Give the extent of all Plasmodium falciparum-infected red blood cells.
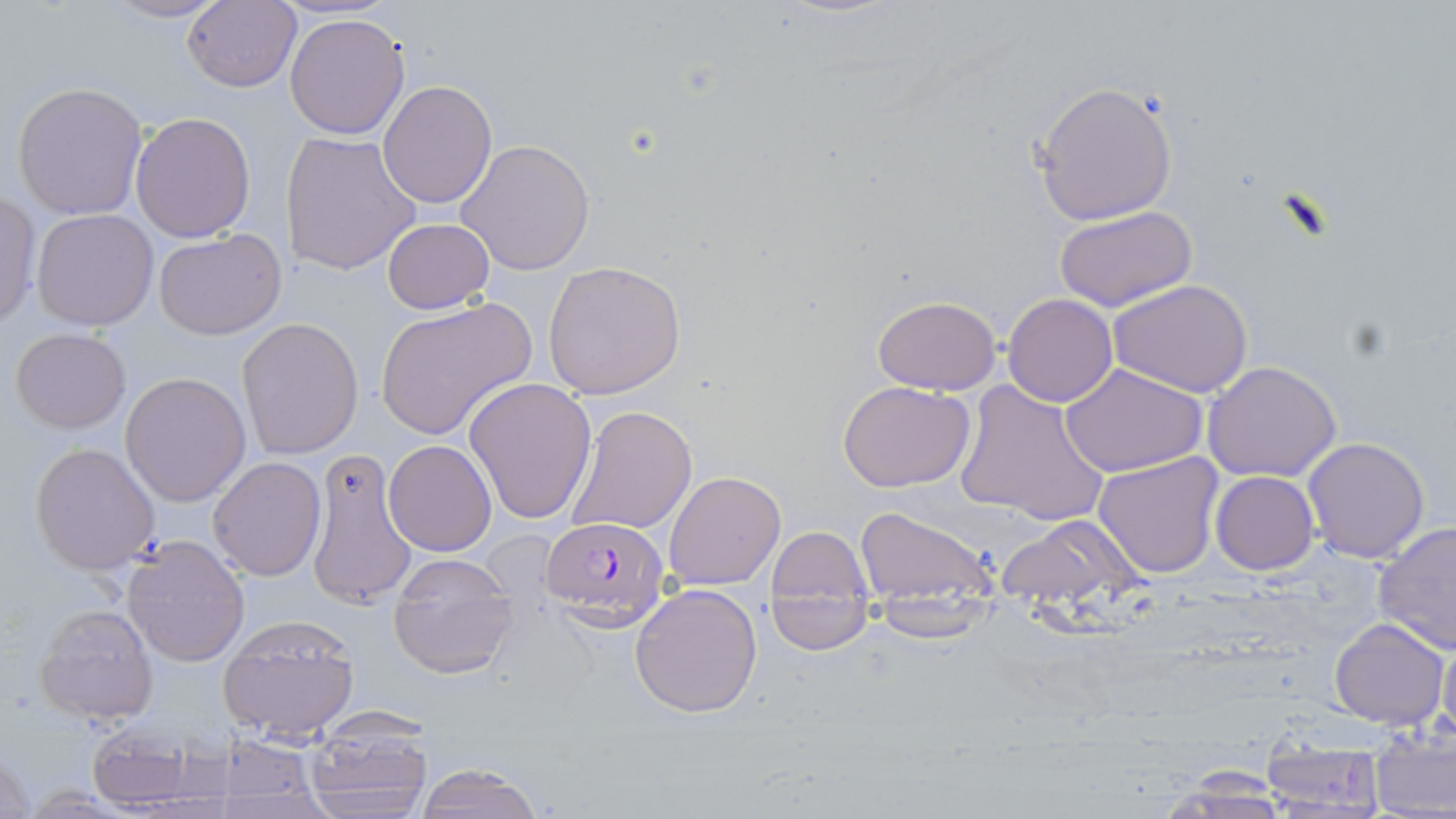
Approximate bounding boxes as named x1/y1/x2/y2 corners in pixels.
Plasmodium falciparum-infected red blood cells: (x1=541, y1=517, x2=670, y2=630).

Uninfected red blood cell locations: (x1=101, y1=1, x2=230, y2=24), (x1=182, y1=1, x2=301, y2=92), (x1=285, y1=12, x2=411, y2=139), (x1=378, y1=79, x2=497, y2=209), (x1=12, y1=81, x2=148, y2=220), (x1=1030, y1=81, x2=1179, y2=227), (x1=130, y1=112, x2=256, y2=242), (x1=282, y1=132, x2=422, y2=276), (x1=456, y1=138, x2=594, y2=275), (x1=0, y1=190, x2=40, y2=330), (x1=1054, y1=204, x2=1198, y2=314), (x1=31, y1=208, x2=160, y2=331), (x1=382, y1=218, x2=494, y2=313), (x1=152, y1=229, x2=286, y2=340), (x1=542, y1=259, x2=687, y2=400), (x1=1108, y1=278, x2=1253, y2=398), (x1=872, y1=294, x2=1001, y2=395), (x1=1003, y1=294, x2=1117, y2=406), (x1=373, y1=297, x2=537, y2=440), (x1=237, y1=318, x2=364, y2=458), (x1=10, y1=327, x2=132, y2=433), (x1=1203, y1=361, x2=1342, y2=482), (x1=1062, y1=364, x2=1208, y2=477), (x1=120, y1=371, x2=251, y2=507), (x1=464, y1=378, x2=598, y2=525), (x1=838, y1=380, x2=976, y2=493), (x1=954, y1=381, x2=1111, y2=528), (x1=564, y1=405, x2=697, y2=536), (x1=1303, y1=436, x2=1432, y2=564), (x1=384, y1=439, x2=496, y2=556), (x1=31, y1=442, x2=161, y2=577), (x1=304, y1=445, x2=418, y2=610), (x1=1093, y1=451, x2=1223, y2=577), (x1=206, y1=457, x2=327, y2=579), (x1=663, y1=470, x2=785, y2=591), (x1=1211, y1=471, x2=1319, y2=576), (x1=852, y1=505, x2=998, y2=610), (x1=997, y1=515, x2=1139, y2=613), (x1=1374, y1=520, x2=1455, y2=654), (x1=763, y1=523, x2=875, y2=648), (x1=120, y1=534, x2=251, y2=667), (x1=386, y1=563, x2=521, y2=680), (x1=630, y1=582, x2=764, y2=719), (x1=869, y1=595, x2=993, y2=642), (x1=34, y1=603, x2=159, y2=726), (x1=217, y1=614, x2=360, y2=744), (x1=1328, y1=617, x2=1449, y2=730), (x1=1438, y1=629, x2=1456, y2=746), (x1=304, y1=718, x2=435, y2=817), (x1=85, y1=721, x2=201, y2=810), (x1=1369, y1=727, x2=1456, y2=819), (x1=1260, y1=736, x2=1388, y2=814), (x1=204, y1=739, x2=333, y2=817), (x1=1, y1=744, x2=36, y2=819), (x1=412, y1=762, x2=548, y2=819). Slide-level diagnosis: Plasmodium falciparum. Captured at 1000x magnification. Thin blood film. Image is 1456×819 pixels. May-Grünwald-Giemsa stain. One field of a larger specimen. Optical microscopy.